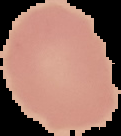 Image is 121×136 pixels. The area outside the segmented cell region is set to black. From a thin blood film. Result: no Plasmodium parasites detected.